Describe the morphology of the erythrocytes.
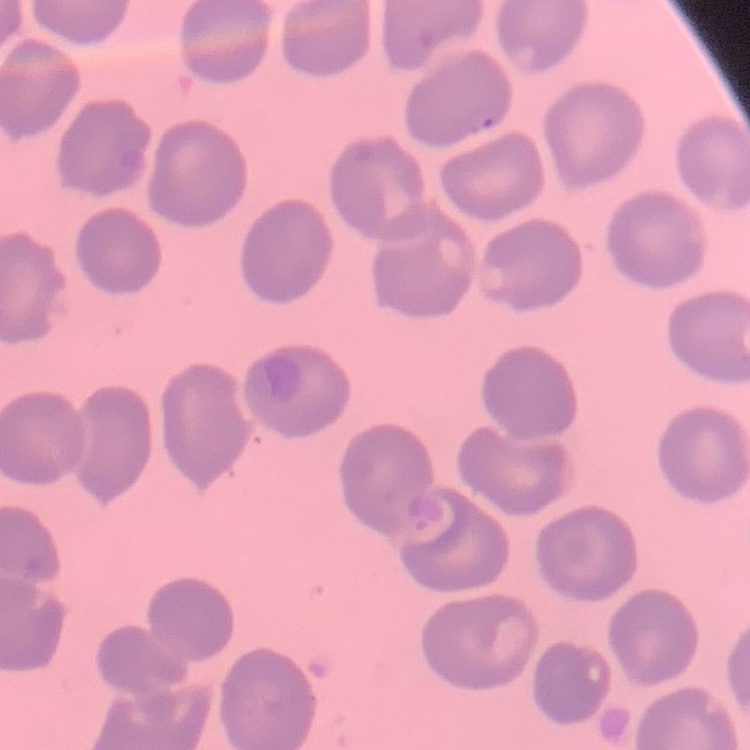

They show no rouleaux formation.

One tile cut from a larger photomicrograph. Stained with either Field's or Giemsa. Thin peripheral smear.